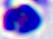

{
  "magnification": "400x",
  "identification": "white blood cell",
  "modality": "photomicrograph"
}